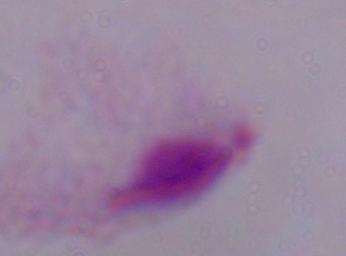
Summary:
  - Identification: trichomonad
  - Modality: photomicrograph
  - Magnification: 1000x